Classify this cell by malaria status.
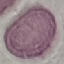
It is uninfected.

{
  "stain": "Giemsa",
  "preparation": "thin smear",
  "image_type": "cell patch, automatically extracted from a larger field of view and resized to 64 × 64 pixels",
  "capture": "smartphone camera at the microscope eyepiece"
}